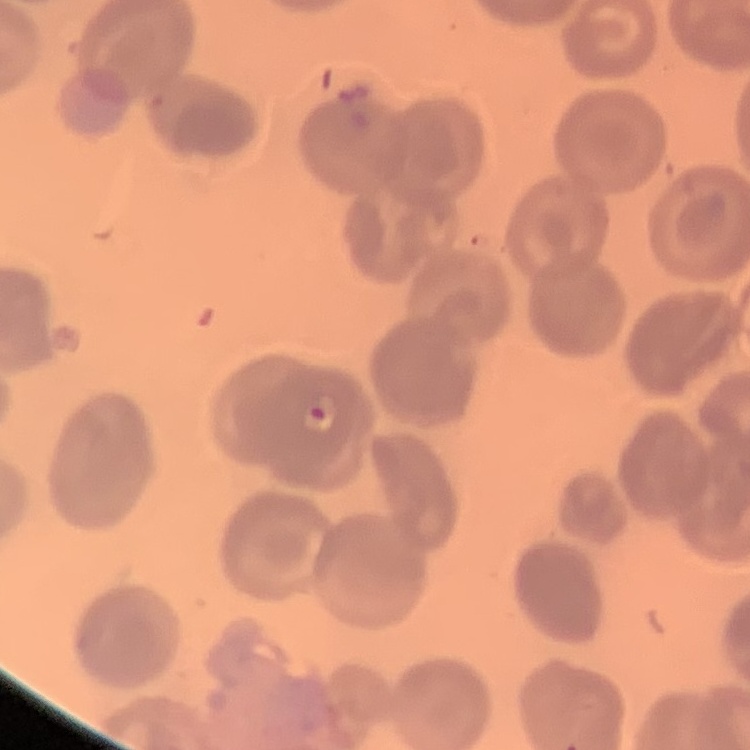

Summary:
  - Erythrocyte morphology: no rouleaux formation
  - Preparation: thin blood film
  - Stain: Field's or Giemsa
  - Image type: one tile cut from a larger photomicrograph